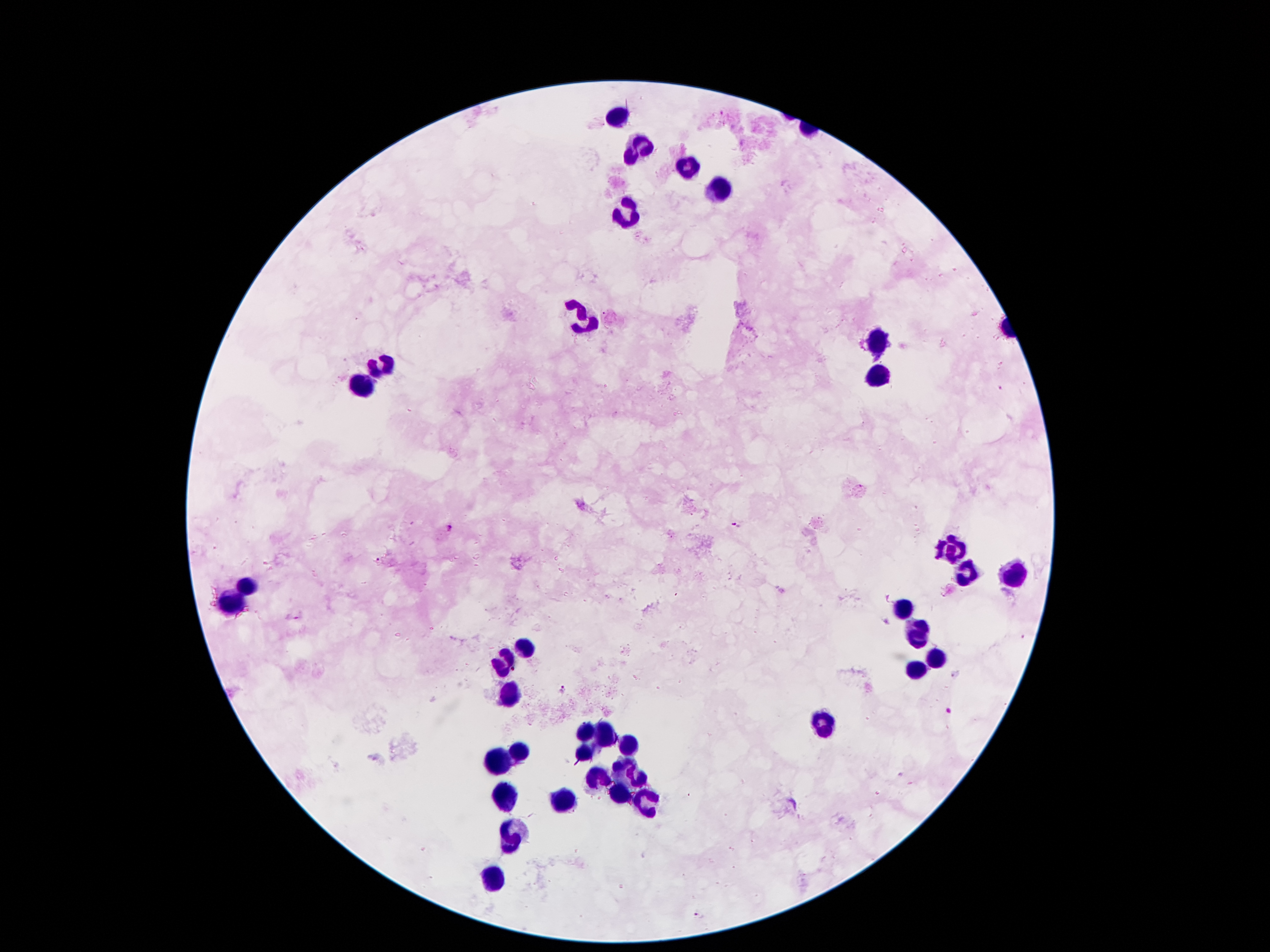
coordinate format = approximate centers as [x, y] in pixels
leukocyte locations = [616, 113], [637, 148], [689, 169], [723, 190], [628, 214], [584, 316], [874, 342], [381, 368], [878, 375], [360, 384], [956, 549], [1014, 572], [246, 585], [229, 604], [902, 609], [918, 627], [523, 650], [939, 659], [504, 663], [916, 670], [511, 692], [824, 723], [588, 729], [605, 734], [626, 746], [519, 753], [584, 755], [502, 760], [623, 767], [597, 777], [637, 778], [504, 797], [617, 797], [565, 800], [644, 804], [513, 835], [490, 877]
malaria parasite locations = [735, 524], [448, 528], [378, 561], [955, 674], [562, 688], [697, 914]
field of view = single
magnification = 100x
preparation = thick peripheral-blood smear
image size = 1270×952 pixels
stain = Giemsa
patient malaria status = infected with Plasmodium falciparum
capture = smartphone camera through the microscope eyepiece